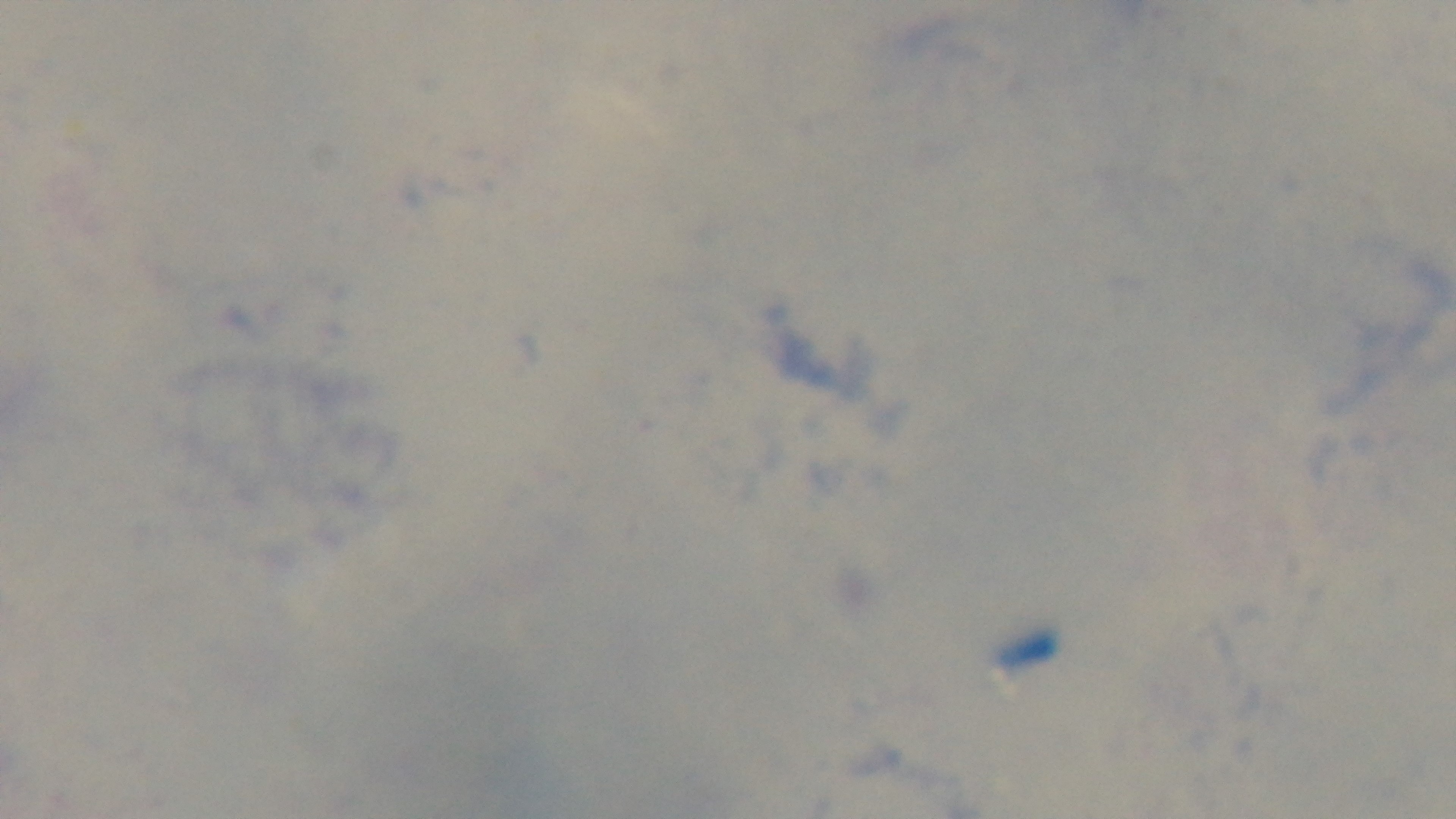

Summary:
  - Field of view: one from the slide
  - Preparation: thick blood film
  - Objective: 100x oil immersion
  - Modality: light microscopy
  - Capture: mounted 4K digital camera
  - Stain: Giemsa
  - Malaria status: uninfected